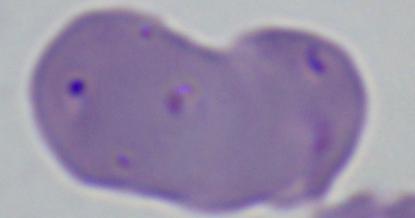
Captured at 1000x magnification. A Babesia parasite is seen. Micrograph.